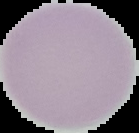 The area outside the segmented cell region is set to black. From a thin blood film. Image is 139×133 pixels. Malaria status: uninfected.